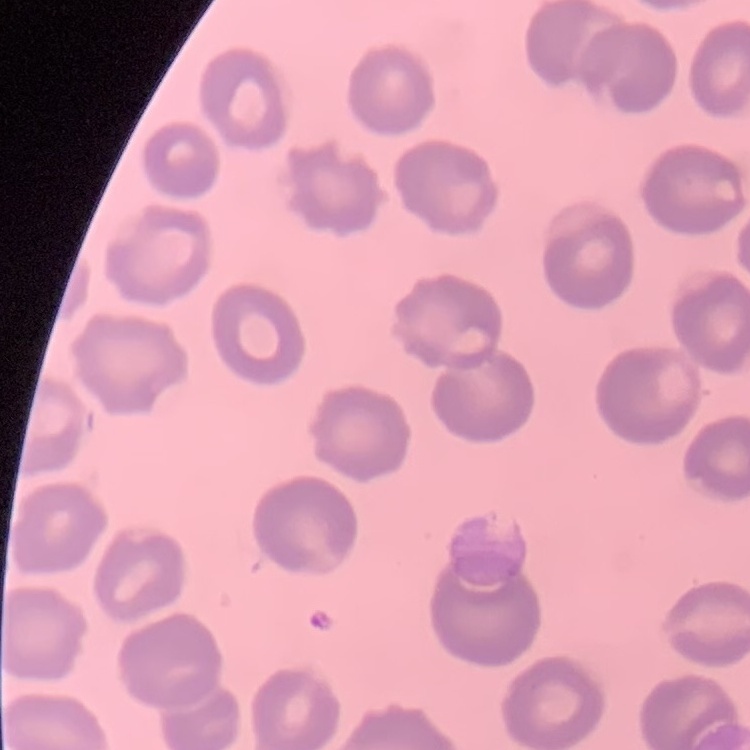 The erythrocytes exhibit no rouleaux formation. Field's or Giemsa stain. Thin blood smear. Square crop of a larger photomicrograph.